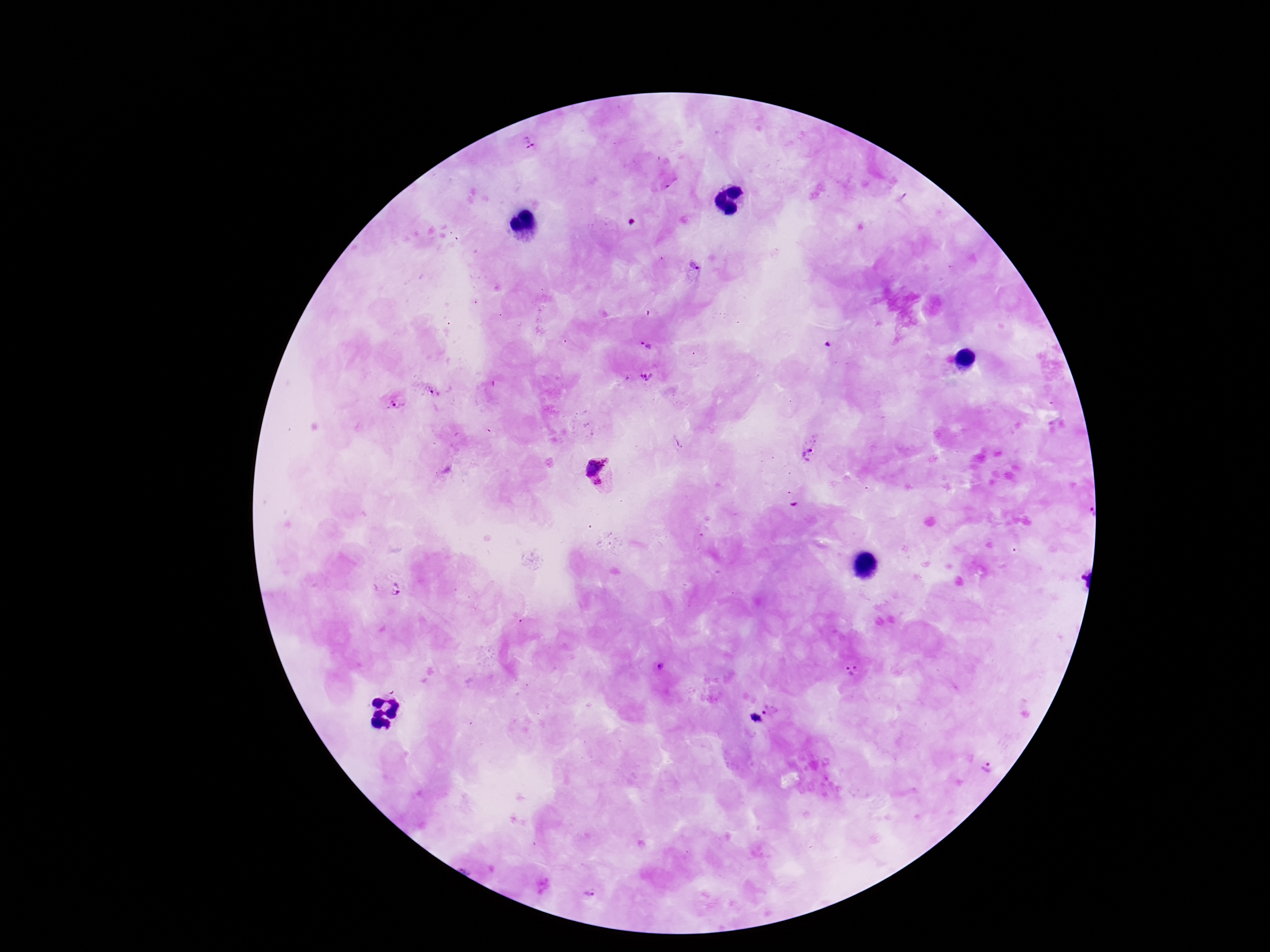
Approximate centers as (x, y) in pixels.
Summary:
  - Plasmodium parasite locations: (528, 147), (692, 268), (645, 346), (646, 378), (394, 404), (811, 455), (599, 475), (393, 589), (851, 672), (773, 708), (753, 720), (982, 769), (590, 890)
  - Magnification: 100x
  - Image size: 1270×952 pixels
  - Patient malaria status: infected
  - Field of view: single
  - Capture: smartphone camera through the microscope eyepiece
  - Stain: Giemsa
  - Preparation: thick blood smear